Locate every uninfected red blood cell.
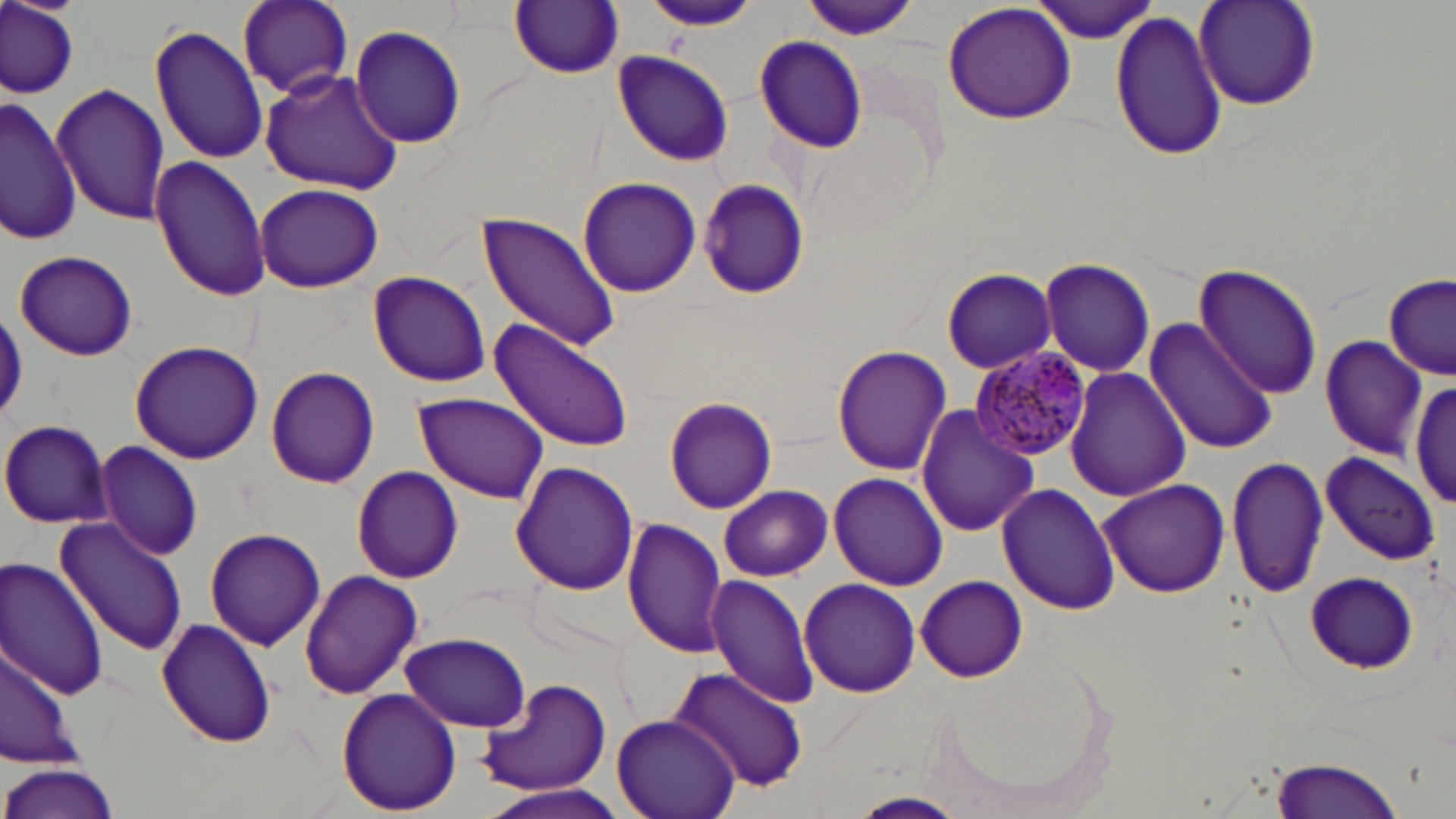
Approximate bounding boxes as (x1, y1, x2, y2) in pixels.
Uninfected red blood cells: (1, 0, 80, 98), (236, 0, 354, 101), (644, 0, 757, 31), (1032, 0, 1162, 42), (511, 1, 624, 78), (802, 1, 918, 41), (942, 1, 1077, 126), (1193, 2, 1321, 111), (1109, 10, 1229, 164), (152, 23, 266, 166), (348, 25, 468, 149), (753, 35, 870, 153), (612, 50, 735, 165), (261, 68, 405, 196), (52, 84, 170, 224), (3, 96, 83, 245), (152, 156, 270, 302), (577, 176, 702, 297), (695, 178, 807, 299), (255, 182, 383, 293), (476, 213, 621, 353), (13, 249, 139, 362), (1038, 257, 1155, 377), (1194, 261, 1324, 399), (942, 268, 1058, 374), (369, 271, 490, 386), (1384, 274, 1455, 379), (1144, 317, 1277, 455), (489, 318, 635, 452), (1320, 336, 1428, 458), (128, 340, 263, 464), (832, 345, 953, 474), (266, 366, 379, 487), (1066, 367, 1190, 502), (1411, 377, 1456, 512), (414, 394, 550, 502), (663, 394, 776, 514), (916, 405, 1038, 538), (0, 419, 113, 528), (94, 442, 205, 560), (1320, 451, 1440, 565), (1225, 452, 1327, 601), (511, 460, 638, 596), (351, 467, 463, 583), (827, 471, 947, 590), (1097, 478, 1230, 598), (997, 483, 1120, 614), (717, 485, 832, 581), (53, 516, 189, 655), (622, 518, 728, 656), (205, 526, 326, 650), (0, 558, 110, 701), (300, 568, 424, 700), (1300, 570, 1423, 674), (705, 572, 819, 710), (915, 575, 1027, 682), (798, 577, 921, 696), (157, 618, 277, 748), (401, 631, 531, 732), (0, 641, 79, 769), (668, 664, 807, 795), (476, 676, 615, 798), (336, 685, 462, 815), (612, 713, 742, 819), (1267, 749, 1410, 819), (0, 762, 120, 819), (478, 781, 629, 819), (849, 791, 970, 818).

slide-level diagnosis = Plasmodium malariae
field of view = single
stain = May-Grünwald-Giemsa
modality = optical microscopy
image size = 1456×819 pixels
magnification = 1000x
preparation = thin blood film
Plasmodium malariae-infected red blood cell locations = approximate bounding boxes as (x1, y1, x2, y2) in pixels: (973, 345, 1092, 461)